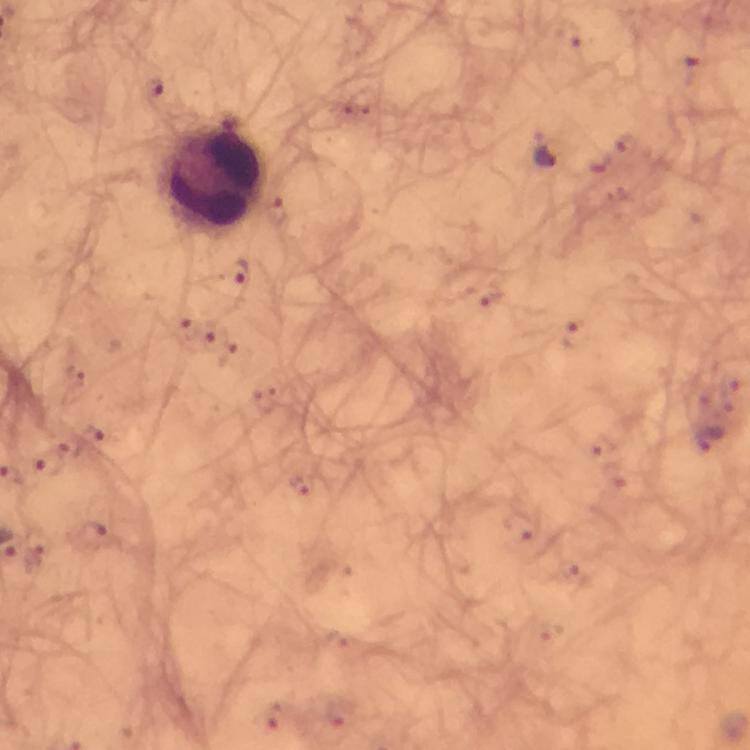

Approximate centers as (x, y) in pixels. Malaria parasite locations: (154, 91), (546, 150), (239, 275), (44, 466), (92, 534). Leukocyte locations: (211, 177). Giemsa stain. From a diagnostic examination for malaria. At 100x magnification. Thick blood film. Smartphone photograph taken through a microscope. A crop from one field of view. Image is 750×750 pixels. Immersion oil was used.